Locate every Plasmodium vivax-infected red blood cell.
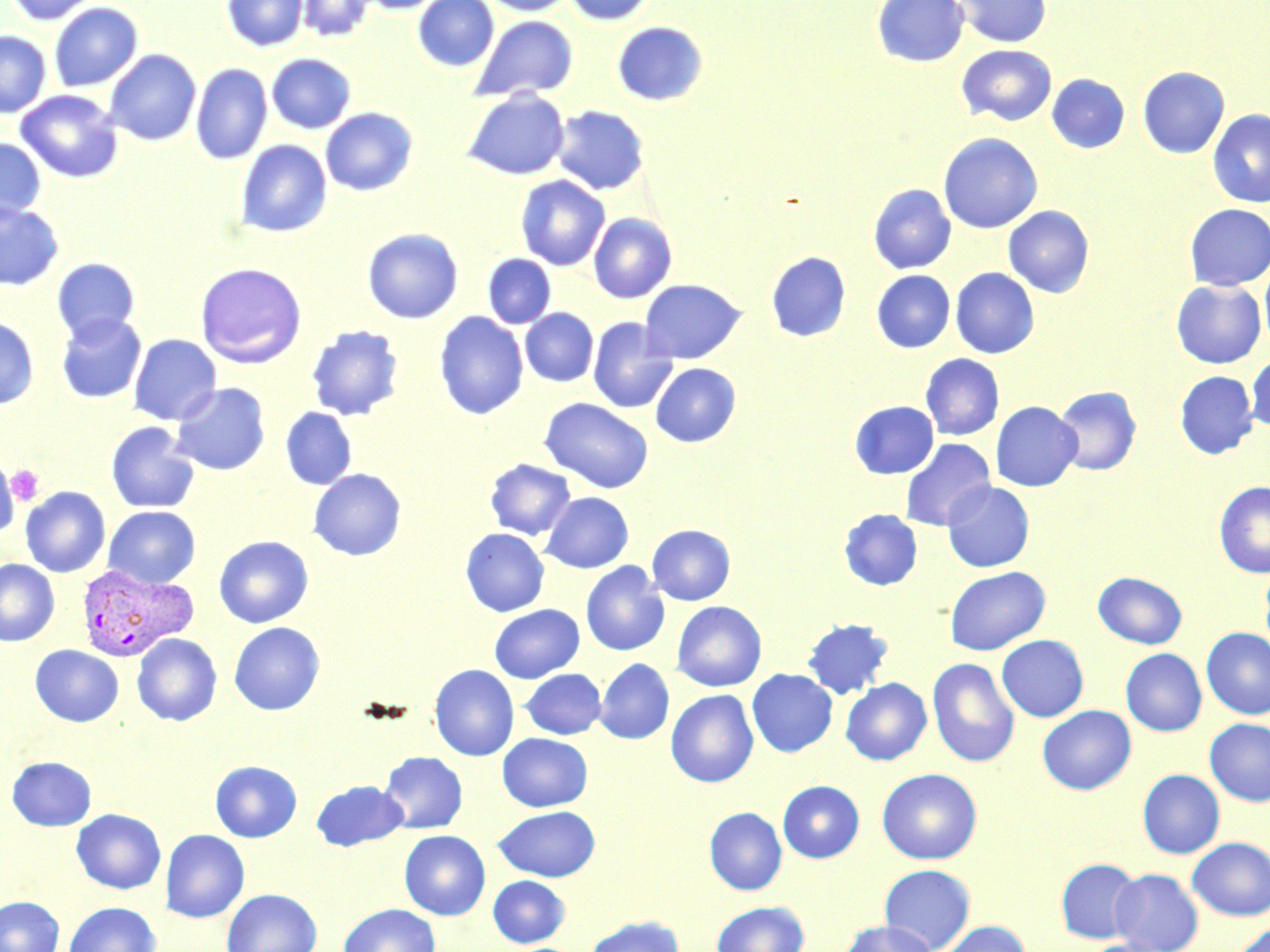

Approximate bounding boxes as (x1, y1, x2, y2) in pixels.
Plasmodium vivax-infected red blood cells: (76, 564, 198, 661).

Summary:
  - Platelet locations: (6, 462, 44, 507)
  - Uninfected red blood cell locations: (5, 0, 101, 26), (222, 0, 308, 52), (297, 0, 373, 43), (355, 0, 445, 14), (412, 0, 499, 72), (482, 0, 576, 16), (564, 0, 656, 26), (871, 0, 969, 67), (953, 0, 1052, 48), (48, 2, 143, 92), (470, 15, 579, 102), (612, 21, 708, 106), (0, 31, 51, 117), (956, 45, 1057, 127), (104, 49, 201, 146), (267, 53, 357, 134), (191, 63, 273, 165), (1137, 66, 1230, 159), (1047, 74, 1130, 154), (15, 89, 123, 184), (462, 89, 569, 180), (551, 105, 649, 195), (320, 107, 418, 196), (1207, 109, 1270, 209), (937, 132, 1043, 234), (0, 138, 46, 223), (236, 139, 332, 237), (515, 174, 610, 271), (868, 184, 956, 274), (0, 202, 65, 291), (1184, 204, 1270, 291), (1003, 205, 1094, 297), (588, 212, 677, 304), (362, 227, 464, 324), (766, 251, 851, 342), (483, 253, 556, 329), (52, 258, 139, 343), (1260, 258, 1270, 352), (194, 262, 307, 368), (950, 267, 1039, 358), (872, 270, 955, 352), (639, 279, 746, 363), (1171, 279, 1267, 368), (520, 308, 598, 386), (434, 311, 528, 420), (56, 314, 147, 404), (0, 315, 39, 409), (588, 317, 678, 414), (306, 325, 403, 421), (128, 334, 221, 425), (920, 353, 1004, 440), (1246, 354, 1270, 431), (650, 363, 741, 447), (1174, 371, 1258, 459), (170, 382, 270, 475), (1053, 386, 1141, 475), (539, 397, 654, 493), (849, 400, 939, 479), (991, 401, 1083, 492), (280, 407, 357, 490), (105, 421, 200, 514), (900, 438, 996, 532), (484, 458, 576, 540), (1, 459, 21, 540), (308, 468, 406, 561), (942, 481, 1034, 572), (1214, 481, 1270, 578), (20, 486, 111, 577), (541, 492, 633, 573), (103, 506, 201, 588), (838, 509, 922, 591), (647, 524, 735, 605), (460, 528, 549, 617), (213, 535, 313, 628), (0, 559, 59, 646), (580, 562, 670, 656), (1260, 562, 1270, 655), (944, 566, 1050, 655), (1093, 571, 1187, 649), (671, 601, 767, 691), (489, 604, 585, 683), (800, 618, 894, 700), (228, 622, 324, 715), (1201, 627, 1270, 720), (132, 633, 222, 726), (996, 634, 1088, 722), (30, 645, 124, 727), (1121, 648, 1207, 736), (927, 657, 1020, 767), (595, 658, 675, 744), (429, 664, 519, 761), (520, 668, 606, 739), (747, 668, 837, 757), (841, 677, 931, 765), (666, 689, 758, 787), (1037, 705, 1136, 795), (1204, 718, 1270, 806), (497, 733, 592, 811), (379, 751, 468, 834), (6, 756, 96, 831), (210, 760, 302, 842), (876, 768, 982, 864), (1137, 769, 1224, 858), (311, 780, 408, 851), (777, 780, 864, 863), (493, 806, 600, 880), (704, 807, 787, 895), (71, 808, 166, 894), (160, 829, 250, 922), (399, 830, 490, 920), (1187, 837, 1270, 920), (1056, 858, 1144, 943), (879, 863, 976, 951), (1110, 868, 1204, 952), (488, 875, 570, 948), (222, 888, 322, 952), (0, 896, 64, 952), (63, 901, 161, 952), (711, 901, 810, 952), (338, 903, 441, 952), (583, 916, 684, 952), (839, 920, 939, 951), (938, 920, 1031, 952), (1231, 922, 1270, 952), (1079, 939, 1173, 952)
  - Slide-level diagnosis: Plasmodium vivax
  - Field of view: single
  - Image size: 1270×952 pixels
  - Preparation: thin blood smear
  - Stain: May-Grünwald-Giemsa
  - Magnification: 1000x
  - Modality: optical microscopy